Point out each Plasmodium parasite.
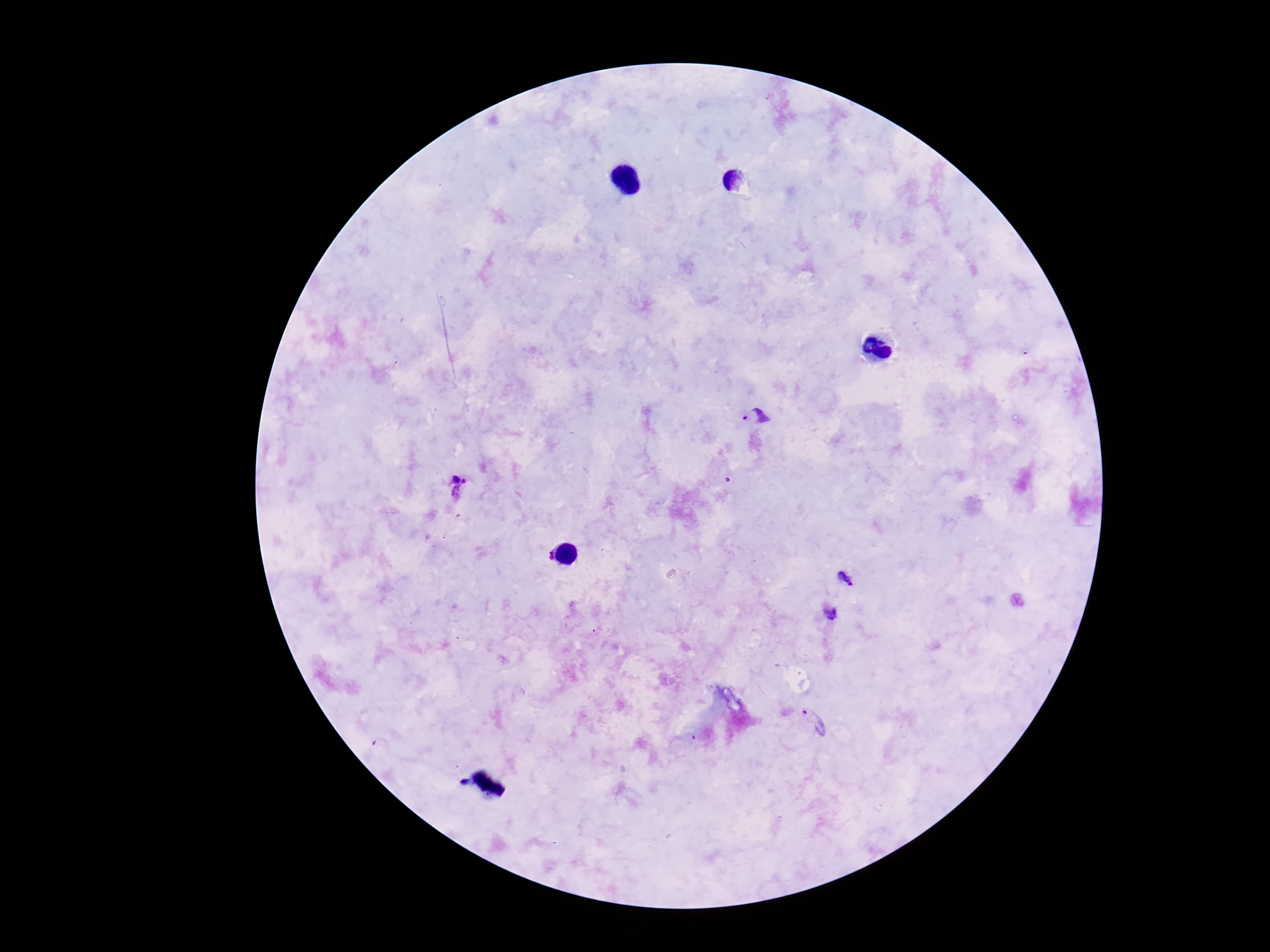

Approximate centers as (x, y) in pixels.
Plasmodium parasites: (758, 419), (457, 488), (548, 555), (845, 580), (831, 613), (814, 722).

Smartphone photograph taken through the microscope eyepiece. 100x magnification. Giemsa-stained preparation. One field from this slide. Patient malaria status: infected. Thick blood film. Image is 1270×952 pixels.